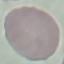

Result: no malaria parasites seen. Thin smear of blood. Photographed with a smartphone camera at the microscope eyepiece. Giemsa stain. Cell patch, automatically extracted from a larger field of view and resized to 64 × 64 pixels.